State which cell type is depicted.
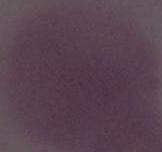
An erythrocyte.

Summary:
  - Modality: photomicrograph
  - Magnification: 1000x